Comment on the morphology of the erythrocytes.
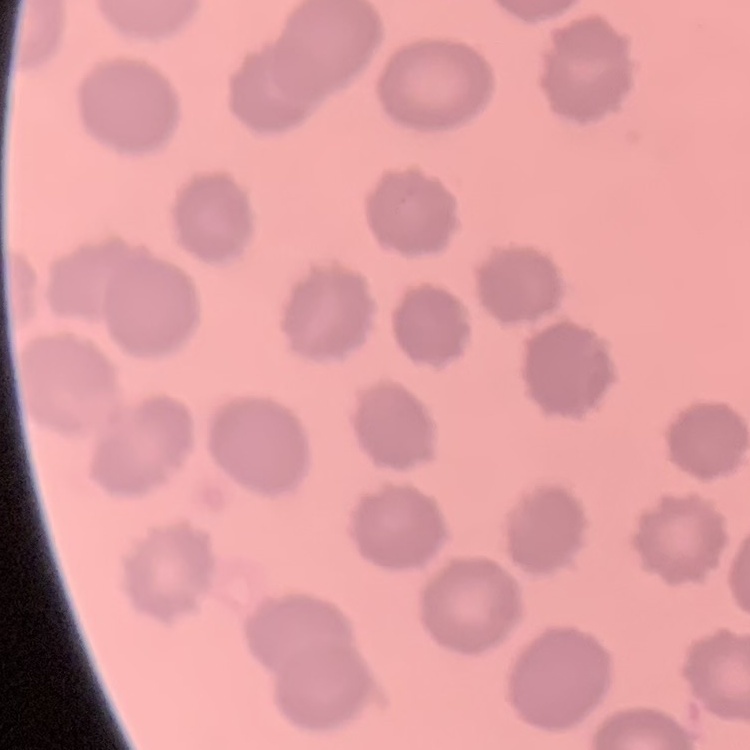

They show no rouleaux formation.

Stained with either Field's or Giemsa. One tile cut from a larger photomicrograph. Thin blood film.